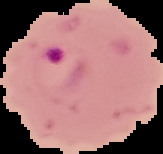

Summary:
  - Image type: segmented cell region with the area outside set to black
  - Image size: 163×154 pixels
  - Malaria status: parasitized
  - Preparation: thin blood film